Assess this cell for malaria.
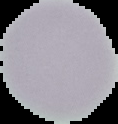

It is uninfected.

The area outside the segmented cell region is set to black. From a thin blood film. Image is 118×124 pixels.